State which cell type is depicted.
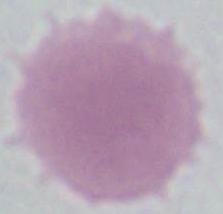

This is an erythrocyte.

modality: micrograph
magnification: 1000x